Classify this cell by malaria status.
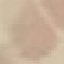

Uninfected.

preparation: thin blood film
capture: smartphone camera at the microscope eyepiece
image_type: cell patch, automatically extracted from a larger field of view and resized to 64 × 64 pixels
stain: Giemsa